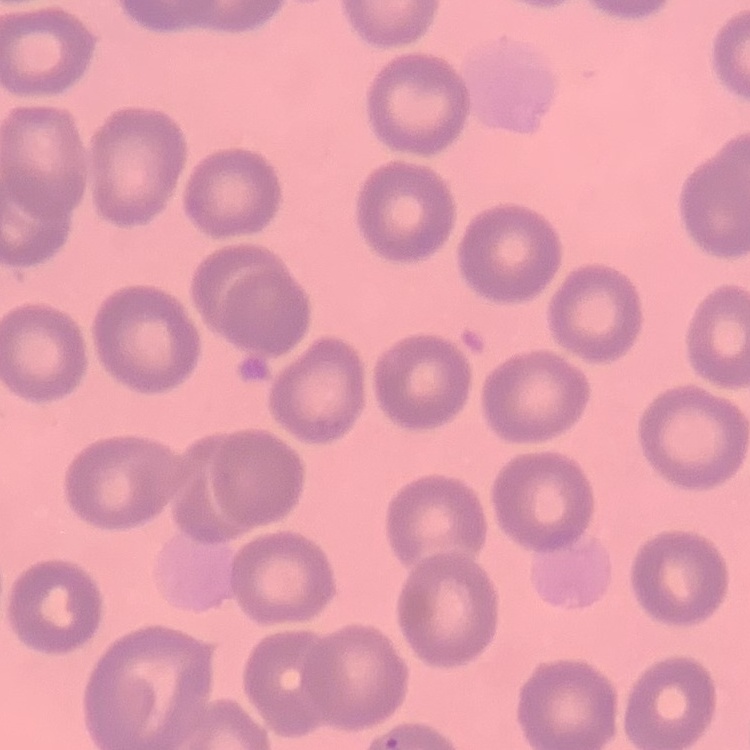 The red blood cells exhibit no rouleaux formation. Field's or Giemsa stain. One tile cut from a larger photomicrograph. Thin blood film.